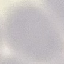

{
  "result": "no malaria parasites seen",
  "preparation": "thin smear",
  "image_type": "automatically extracted cell patch, resized to 64 × 64 pixels",
  "stain": "Giemsa",
  "capture": "smartphone through the microscope eyepiece"
}